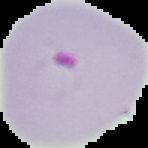
Cell region segmented out of the field of view; the surrounding area is masked to black. Image is 148×148 pixels. Result: malaria parasites identified. From a thin blood film.